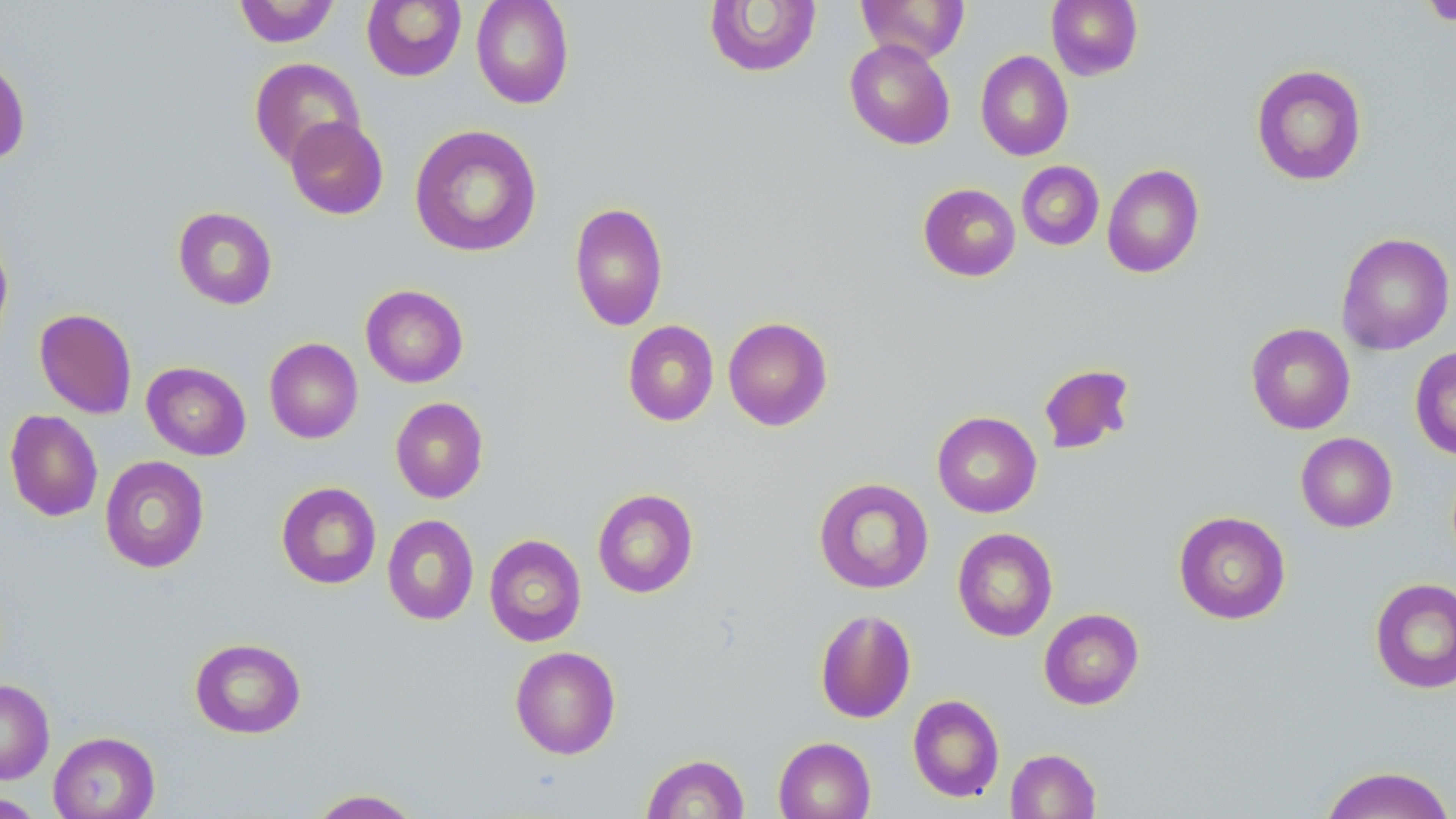
Summary:
  - Coordinate format: approximate bounding boxes as (x1, y1, x2, y2) in pixels
  - Uninfected red blood cell locations: (233, 0, 341, 47), (362, 0, 466, 82), (471, 0, 574, 109), (856, 0, 970, 63), (1046, 0, 1143, 80), (703, 1, 823, 78), (1422, 1, 1456, 27), (844, 38, 956, 150), (975, 50, 1074, 161), (0, 55, 31, 165), (249, 57, 365, 168), (1250, 63, 1367, 186), (285, 116, 389, 220), (409, 123, 543, 257), (1016, 161, 1104, 251), (1102, 164, 1204, 278), (918, 183, 1021, 282), (569, 202, 668, 331), (173, 206, 278, 310), (1335, 232, 1455, 355), (0, 234, 13, 350), (360, 284, 468, 388), (33, 308, 137, 419), (723, 316, 833, 431), (623, 320, 719, 426), (1246, 322, 1356, 435), (264, 338, 363, 444), (1409, 346, 1456, 460), (142, 361, 251, 460), (1038, 363, 1136, 455), (390, 397, 489, 503), (4, 409, 103, 522), (932, 411, 1042, 518), (1296, 431, 1397, 532), (99, 455, 210, 573), (813, 477, 934, 595), (276, 481, 382, 589), (592, 487, 698, 598), (1173, 511, 1291, 624), (382, 514, 479, 626), (952, 527, 1058, 642), (484, 534, 586, 647), (1369, 577, 1456, 694), (814, 608, 916, 723), (1039, 608, 1144, 709), (189, 637, 306, 739), (510, 646, 621, 759), (0, 679, 55, 784), (907, 694, 1004, 802), (48, 731, 160, 819), (773, 737, 875, 819), (1005, 748, 1100, 819), (642, 753, 749, 818), (1319, 765, 1455, 819), (306, 788, 423, 818), (0, 792, 46, 817)
  - Platelet locations: (1422, 0, 1456, 26)
  - Slide-level diagnosis: no evidence of blood parasites
  - Preparation: thin blood smear
  - Magnification: 1000x
  - Modality: optical microscopy
  - Stain: May-Grünwald-Giemsa
  - Image size: 1456×819 pixels
  - Field of view: one of a larger specimen